Give the preparation type.
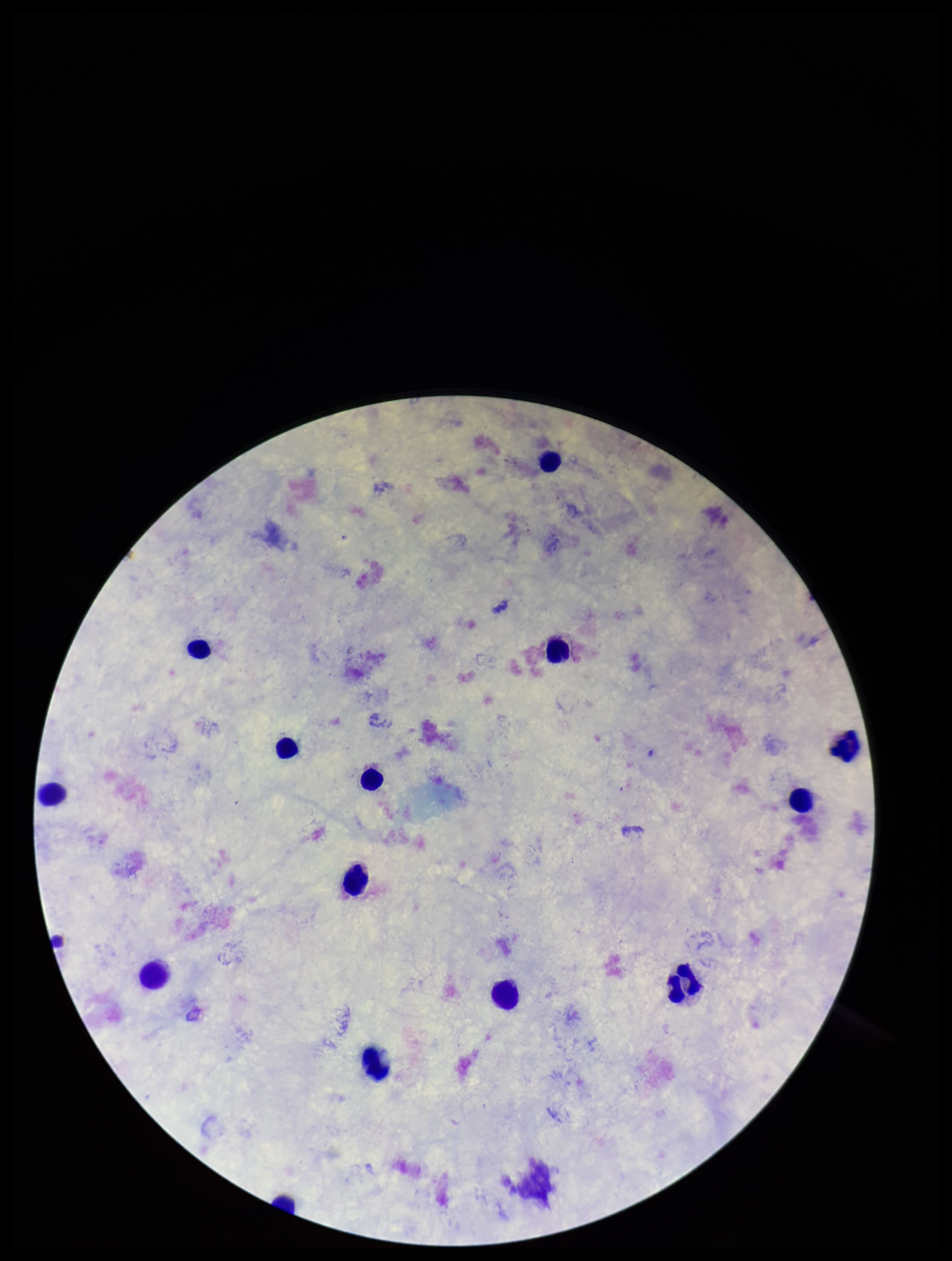

It is a thick blood smear.

Patient malaria status: negative. Stained with Giemsa. Leukocyte count: 14. Photographed through the microscope eyepiece with a smartphone camera. Parasite count: 0. Single field of view. Image is 952×1261 pixels. Plasmodium parasites: none seen.